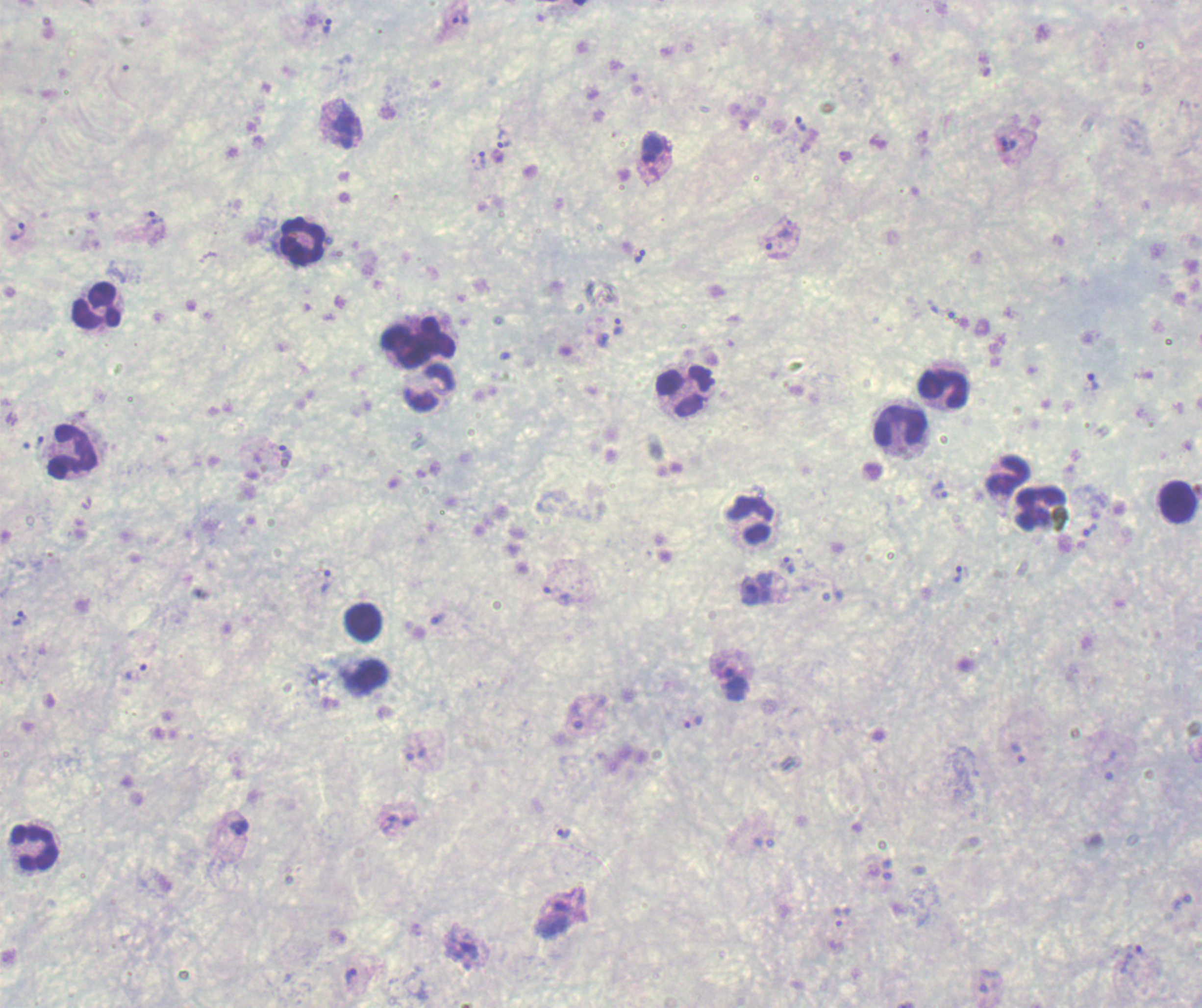

Approximate object centers, in pixels from the top-left corner. Leukocyte locations: (x=299, y=239), (x=95, y=304), (x=416, y=340), (x=429, y=389), (x=943, y=391), (x=685, y=392), (x=901, y=428), (x=72, y=450), (x=1008, y=476), (x=1176, y=502), (x=1039, y=509), (x=750, y=519), (x=363, y=621), (x=368, y=676), (x=34, y=849). Trophozoite locations: (x=461, y=21), (x=327, y=26), (x=800, y=123), (x=346, y=129), (x=504, y=139), (x=1007, y=145), (x=479, y=161), (x=155, y=218), (x=787, y=230), (x=17, y=231), (x=773, y=249), (x=639, y=256), (x=617, y=327), (x=1092, y=382), (x=285, y=451), (x=939, y=491), (x=1089, y=529), (x=789, y=566), (x=958, y=574), (x=326, y=582), (x=750, y=589), (x=557, y=595), (x=18, y=619), (x=438, y=619), (x=136, y=671), (x=734, y=684), (x=692, y=722), (x=1018, y=753), (x=416, y=754), (x=1110, y=766), (x=389, y=823), (x=239, y=827), (x=564, y=834), (x=841, y=917), (x=1131, y=959), (x=351, y=976). Previously used in a real diagnosis. Image is 1202×1008 pixels. 100x magnification. Thick blood film. Single field of view. Romanowsky-stained preparation. Result: positive for Plasmodium parasites. Background quality: poor.